Outline every leukocyte.
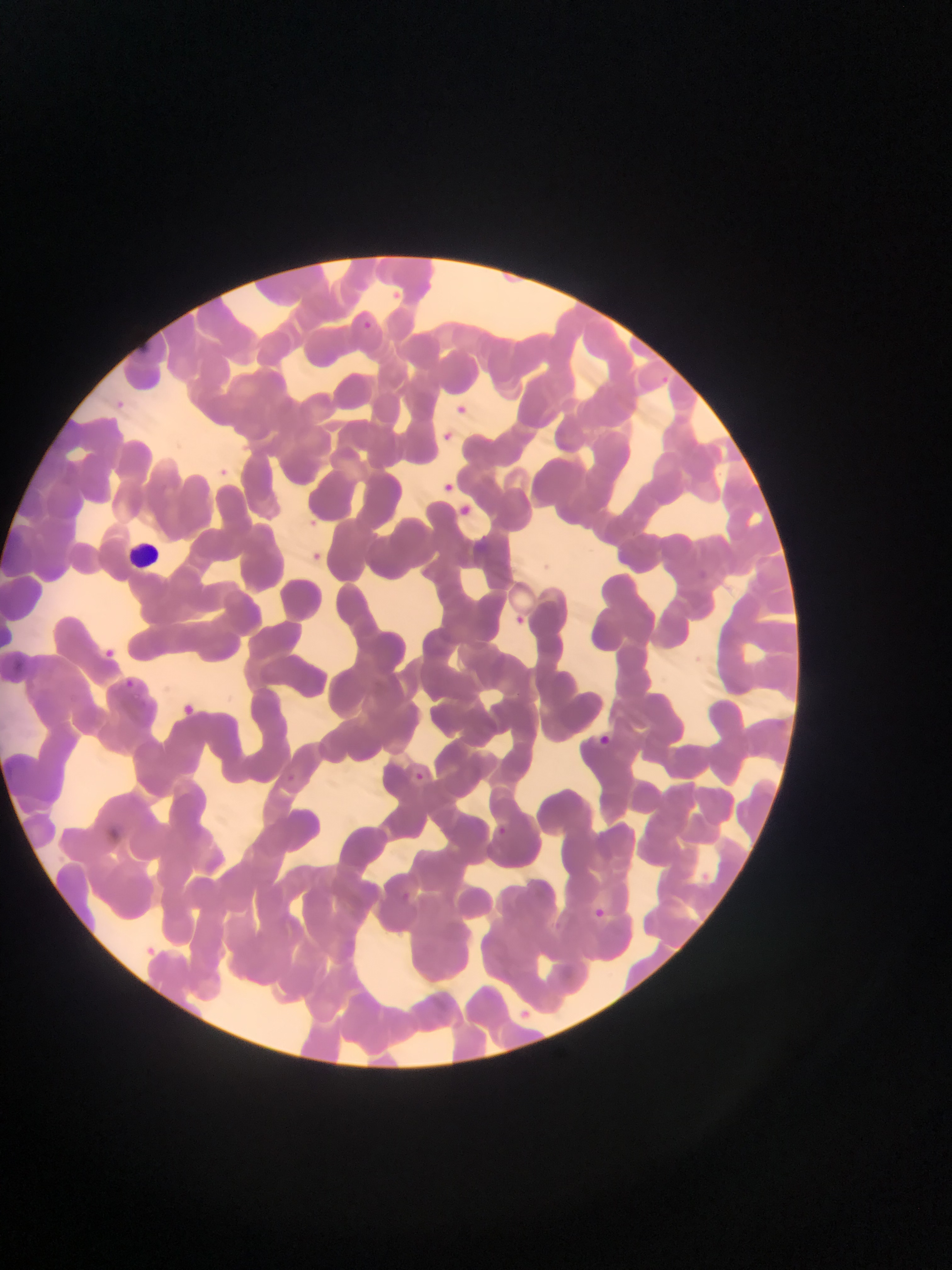
Approximate bounding boxes as left top right bottom in pixels.
Leukocytes: 121 530 177 576.

Malaria parasite locations: 352 315 377 337; 453 400 468 417; 442 430 457 448; 442 480 454 500; 456 501 480 520; 304 514 320 531; 479 538 497 570; 306 552 322 570; 511 612 525 628; 99 639 116 660; 124 677 142 693; 184 702 200 718; 597 731 613 749; 412 764 440 794; 495 821 523 851. Single field of view. Image is 952×1270 pixels. Thin blood smear. Mobile-phone photograph taken through the microscope. Sample from Ghana.